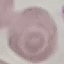 Result: no malaria parasites seen. Photographed with a smartphone camera at the microscope eyepiece. Automatically extracted cell patch, resized to 64 × 64 pixels. Thin smear of blood. Giemsa stain.